Name the parasite shown.
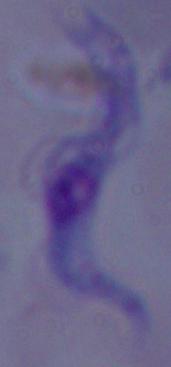

A trypanosome.

Summary:
  - Modality: photomicrograph
  - Magnification: 1000x